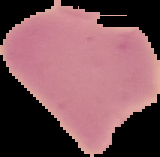
result = no Plasmodium parasites detected
preparation = thin blood smear
image size = 160×157 pixels
image type = segmented cell region with the area outside set to black